Assess the morphology of the erythrocytes.
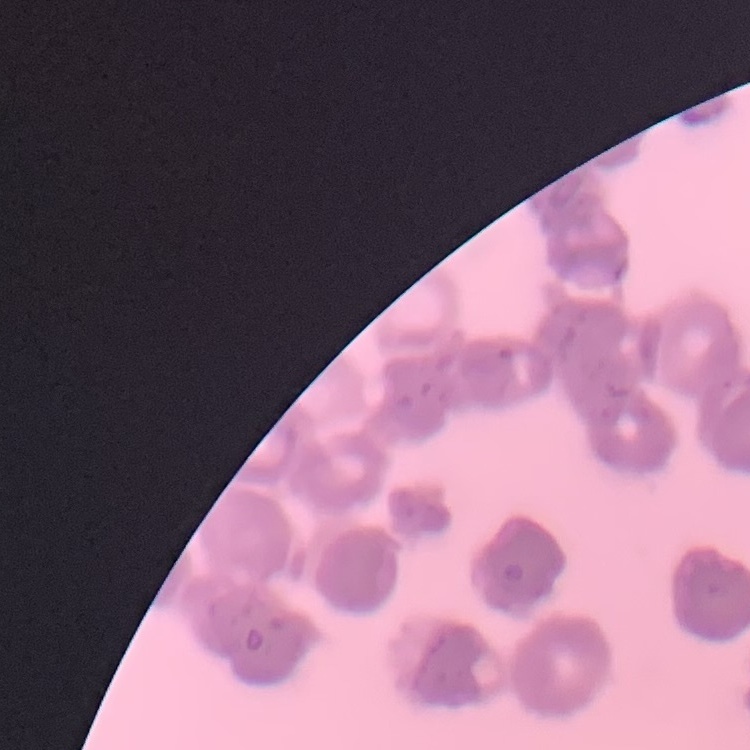
They show rouleaux formation.

Summary:
  - Preparation: thin peripheral smear
  - Stain: Field's or Giemsa
  - Image type: square crop of a larger photomicrograph